Classify this cell by malaria status.
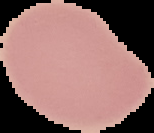

It is uninfected.

Summary:
  - Image size: 154×133 pixels
  - Image type: cell region segmented out of the field of view; surrounding area masked to black
  - Preparation: thin blood film